Report the malaria status of this cell.
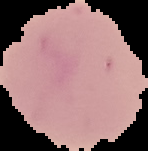

Uninfected.

From a thin blood smear. Image is 148×151 pixels. Cell region segmented out of the field of view; the surrounding area is masked to black.